Comment on the morphology of the erythrocytes.
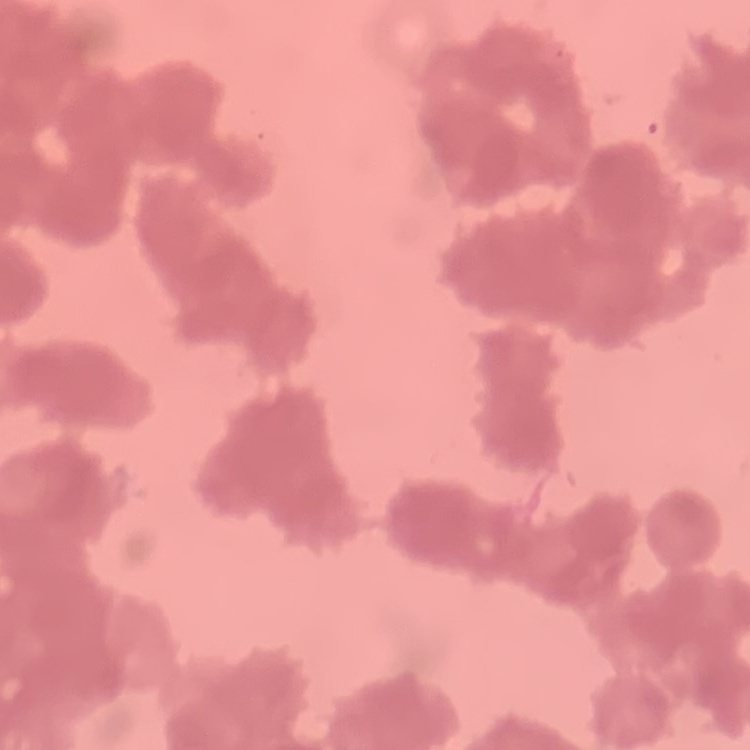

Rouleaux formation.

{
  "preparation": "thin blood film",
  "image_type": "one tile cut from a larger photomicrograph",
  "stain": "Field's or Giemsa"
}